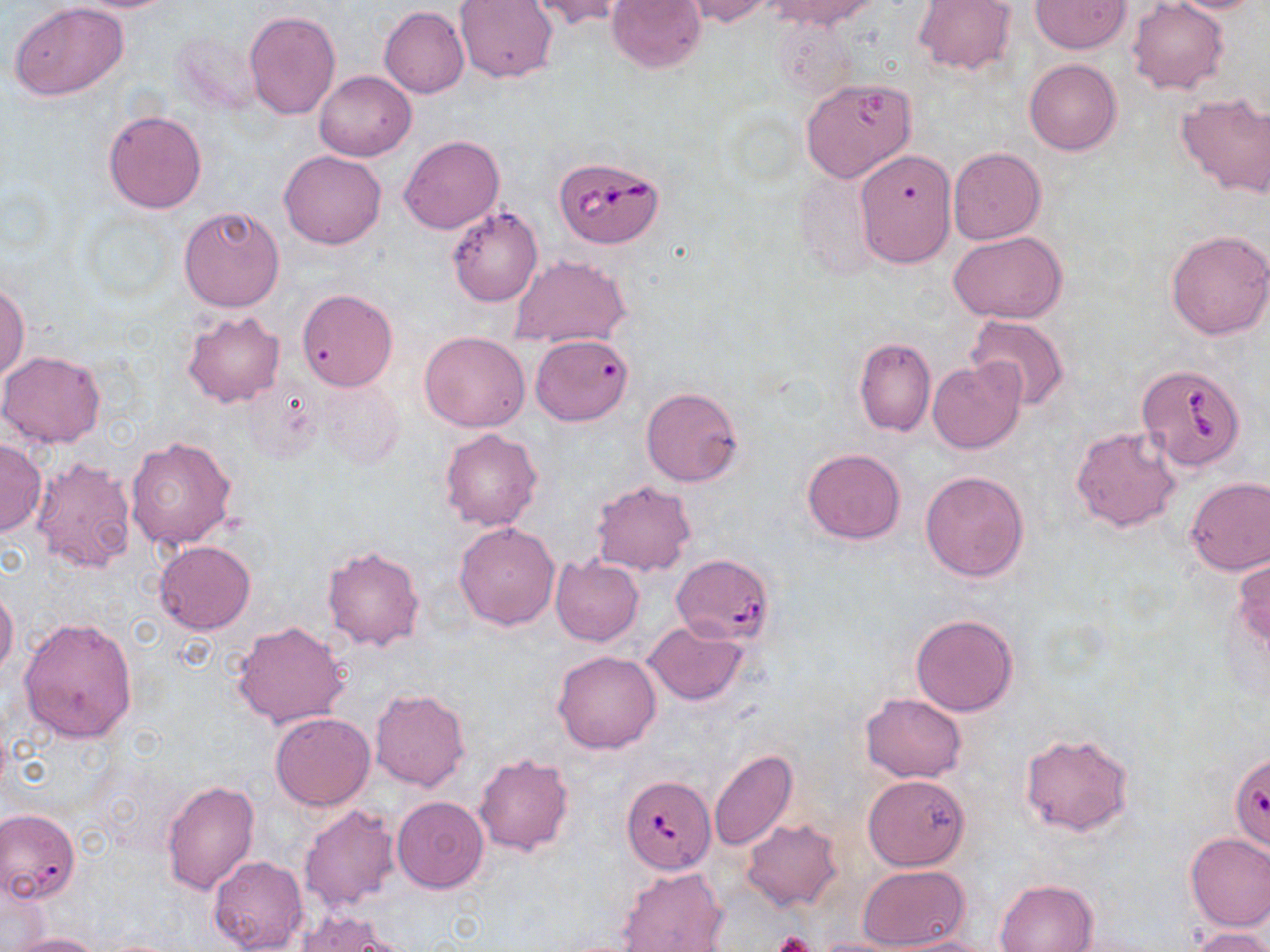

Summary:
  - Coordinate format: approximate bounding boxes as (x1, y1, x2, y2) in pixels
  - Uninfected red blood cell locations: (53, 0, 188, 13), (526, 0, 634, 30), (606, 0, 706, 73), (761, 0, 883, 30), (914, 0, 1015, 74), (1128, 0, 1229, 94), (1163, 0, 1270, 13), (454, 1, 558, 83), (681, 1, 777, 25), (1029, 1, 1131, 53), (9, 2, 130, 101), (379, 5, 470, 97), (244, 10, 341, 120), (173, 25, 263, 116), (1024, 59, 1123, 156), (314, 71, 416, 161), (800, 77, 919, 184), (1176, 93, 1270, 197), (104, 109, 208, 214), (399, 135, 504, 233), (948, 147, 1045, 243), (853, 149, 956, 267), (279, 150, 387, 249), (794, 169, 882, 280), (177, 205, 285, 313), (447, 206, 542, 307), (949, 230, 1067, 325), (1166, 230, 1270, 339), (510, 254, 630, 348), (0, 283, 28, 382), (296, 289, 397, 391), (182, 310, 285, 408), (964, 313, 1069, 410), (419, 331, 530, 431), (531, 333, 634, 425), (853, 335, 935, 437), (0, 350, 106, 448), (927, 360, 1025, 454), (241, 378, 322, 460), (319, 381, 405, 470), (641, 386, 744, 487), (1071, 426, 1182, 531), (440, 428, 542, 530), (125, 436, 238, 552), (0, 439, 45, 535), (802, 448, 906, 544), (30, 458, 138, 575), (920, 471, 1030, 582), (1184, 476, 1270, 576), (591, 481, 697, 576), (454, 521, 559, 629), (154, 541, 256, 634), (323, 544, 426, 650), (549, 555, 644, 646), (1232, 555, 1270, 655), (0, 586, 19, 680), (910, 613, 1019, 716), (18, 616, 138, 742), (232, 620, 352, 729), (643, 620, 747, 706), (552, 650, 662, 754), (370, 687, 471, 792), (860, 692, 968, 783), (270, 713, 375, 811), (1019, 732, 1134, 837), (709, 749, 798, 851), (473, 751, 575, 857), (864, 774, 970, 870), (161, 779, 260, 894), (392, 797, 489, 893), (298, 804, 400, 915), (0, 808, 79, 904), (740, 819, 843, 913), (1185, 832, 1270, 930), (209, 854, 307, 951), (616, 865, 728, 951), (858, 865, 970, 950), (995, 879, 1098, 952), (294, 911, 402, 951), (1189, 928, 1269, 952), (6, 932, 107, 952), (885, 935, 1000, 952), (807, 937, 927, 952)
  - Babesia divergens-infected red blood cell locations: (553, 154, 664, 249), (1132, 365, 1246, 474), (673, 554, 775, 644), (620, 775, 717, 875)
  - Platelet locations: (770, 931, 816, 952)
  - Slide-level diagnosis: Babesia divergens
  - Magnification: 1000x
  - Preparation: thin blood film
  - Field of view: one of a larger specimen
  - Image size: 1270×952 pixels
  - Modality: light microscopy
  - Stain: May-Grünwald-Giemsa